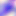

identification = Toxoplasma gondii
modality = micrograph
magnification = 400x